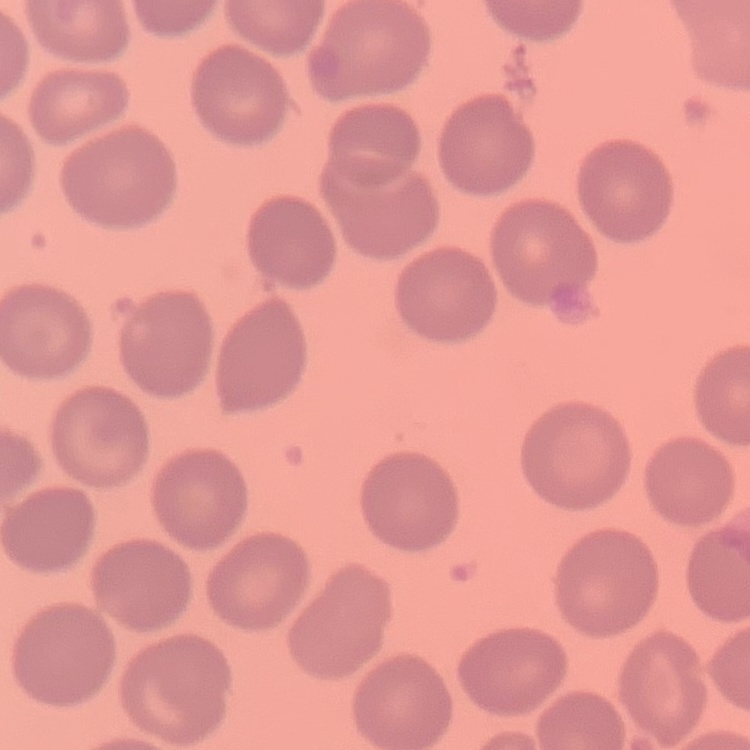
The red blood cells exhibit no rouleaux formation. Stained with either Field's or Giemsa. Thin peripheral smear. Square crop of a larger photomicrograph.